Assess this cell for malaria.
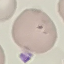
It is parasitized.

Summary:
  - Stain: Giemsa
  - Image type: automatically extracted cell patch, resized to 64 × 64 pixels
  - Capture: smartphone camera at the microscope eyepiece
  - Preparation: thin blood smear